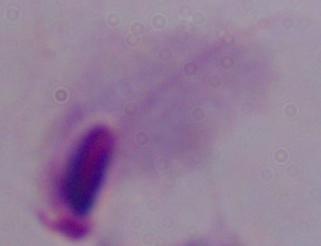
modality: photomicrograph
identification: trichomonad
magnification: 1000x